Identify the blood parasite species.
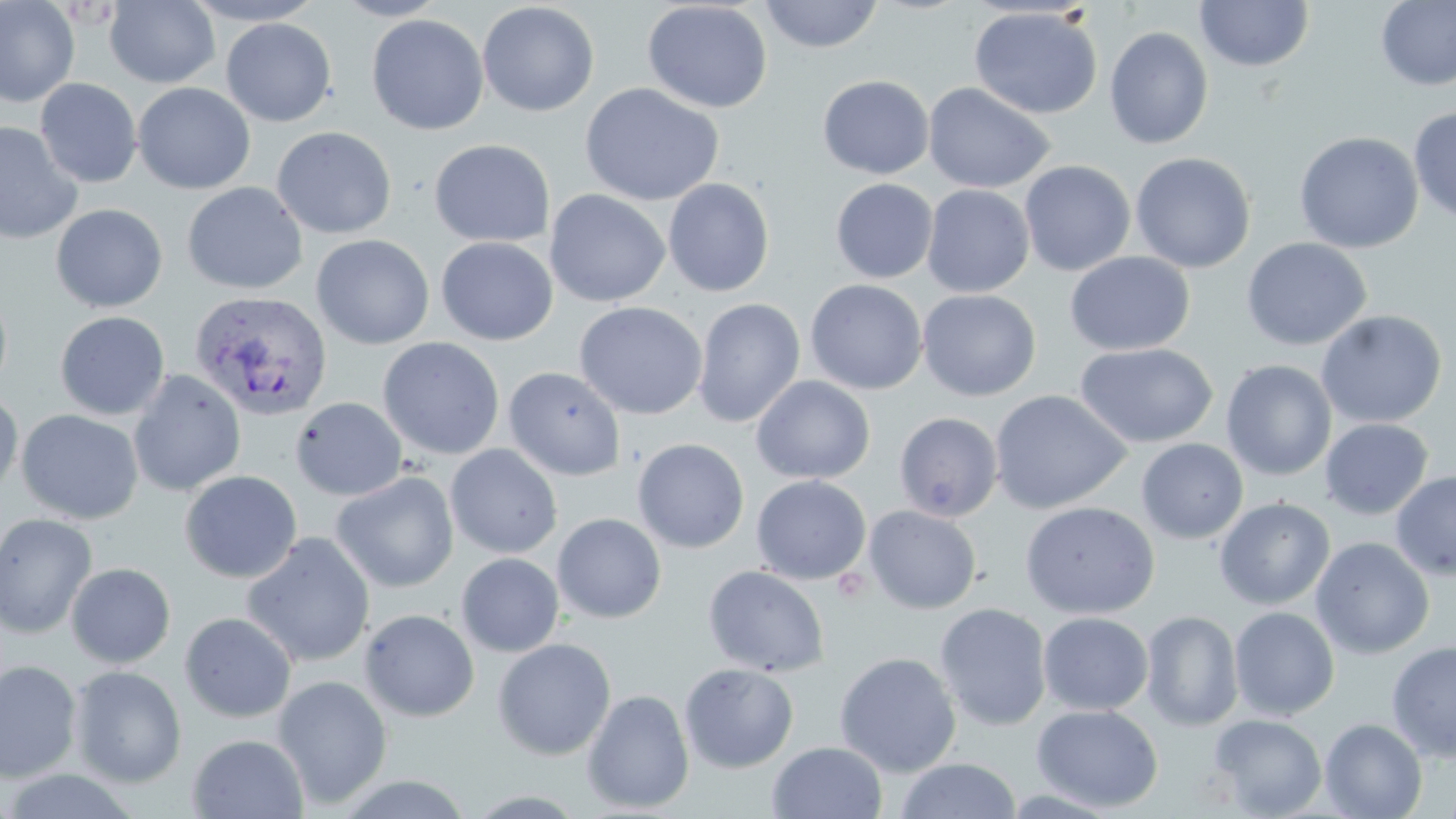

Plasmodium vivax.

Summary:
  - Coordinate format: approximate bounding boxes as (x1,y1)-(x2,y2) corner pairs in pixels
  - Plasmodium vivax-infected red blood cell locations: (189,291)-(331,421)
  - Uninfected red blood cell locations: (0,0)-(79,108), (104,0)-(220,88), (181,0)-(328,26), (332,0)-(450,21), (759,0)-(884,53), (1375,0)-(1456,91), (642,1)-(773,114), (1195,1)-(1314,72), (477,2)-(600,117), (112,3)-(240,170), (969,6)-(1103,119), (366,14)-(489,135), (220,18)-(336,126), (1104,26)-(1214,149), (818,74)-(934,179), (35,78)-(142,188), (923,81)-(1056,193), (133,82)-(255,194), (580,83)-(724,207), (1408,105)-(1456,223), (0,120)-(83,245), (271,126)-(397,239), (1294,131)-(1424,254), (429,139)-(555,247), (1130,152)-(1256,273), (1019,160)-(1136,276), (662,177)-(775,297), (830,178)-(938,283), (181,181)-(307,295), (922,184)-(1035,298), (544,189)-(671,307), (51,203)-(168,313), (311,234)-(434,350), (436,237)-(558,345), (1241,237)-(1373,351), (1064,251)-(1194,356), (805,279)-(927,395), (0,282)-(13,397), (916,289)-(1041,401), (692,298)-(806,428), (573,302)-(708,420), (1315,310)-(1448,429), (55,311)-(170,420), (377,337)-(505,461), (1075,342)-(1218,448), (1221,360)-(1337,481), (503,366)-(627,482), (128,369)-(246,497), (751,375)-(875,484), (0,390)-(23,499), (989,390)-(1132,514), (290,396)-(409,501), (16,409)-(143,524), (894,412)-(1003,522), (1320,418)-(1433,520), (632,438)-(750,554), (1136,438)-(1248,544), (445,444)-(563,559), (179,470)-(302,583), (1390,470)-(1456,581), (331,472)-(459,593), (751,475)-(872,585), (1214,497)-(1335,610), (1020,501)-(1159,619), (863,505)-(981,614), (0,513)-(98,638), (552,513)-(666,624), (242,532)-(376,668), (1310,536)-(1435,659), (456,553)-(564,657), (66,562)-(176,668), (703,565)-(830,677), (934,603)-(1052,731), (1229,607)-(1340,720), (360,608)-(480,722), (1140,610)-(1243,731), (179,611)-(297,723), (1038,612)-(1154,715), (492,638)-(616,761), (1386,640)-(1456,761), (834,652)-(962,777), (0,660)-(82,783), (679,662)-(799,773), (69,665)-(187,788), (272,675)-(393,809), (582,689)-(694,813), (1032,704)-(1164,812), (1208,714)-(1327,818), (1320,718)-(1427,819), (187,734)-(309,818), (767,741)-(887,819), (895,758)-(1021,818), (334,774)-(475,818)
  - Field of view: single
  - Stain: May-Grünwald-Giemsa
  - Modality: light microscopy
  - Magnification: 1000x
  - Image size: 1456×819 pixels
  - Preparation: thin blood smear